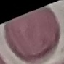

Malaria status: uninfected. Giemsa stain. Photographed with a smartphone camera at the microscope eyepiece. Thin smear of blood. Cell patch, automatically extracted from a larger field of view and resized to 64 × 64 pixels.